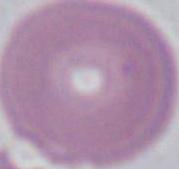
Micrograph. A red blood cell is shown. 1000x magnification.